Give the extent of all uninfected red blood cells.
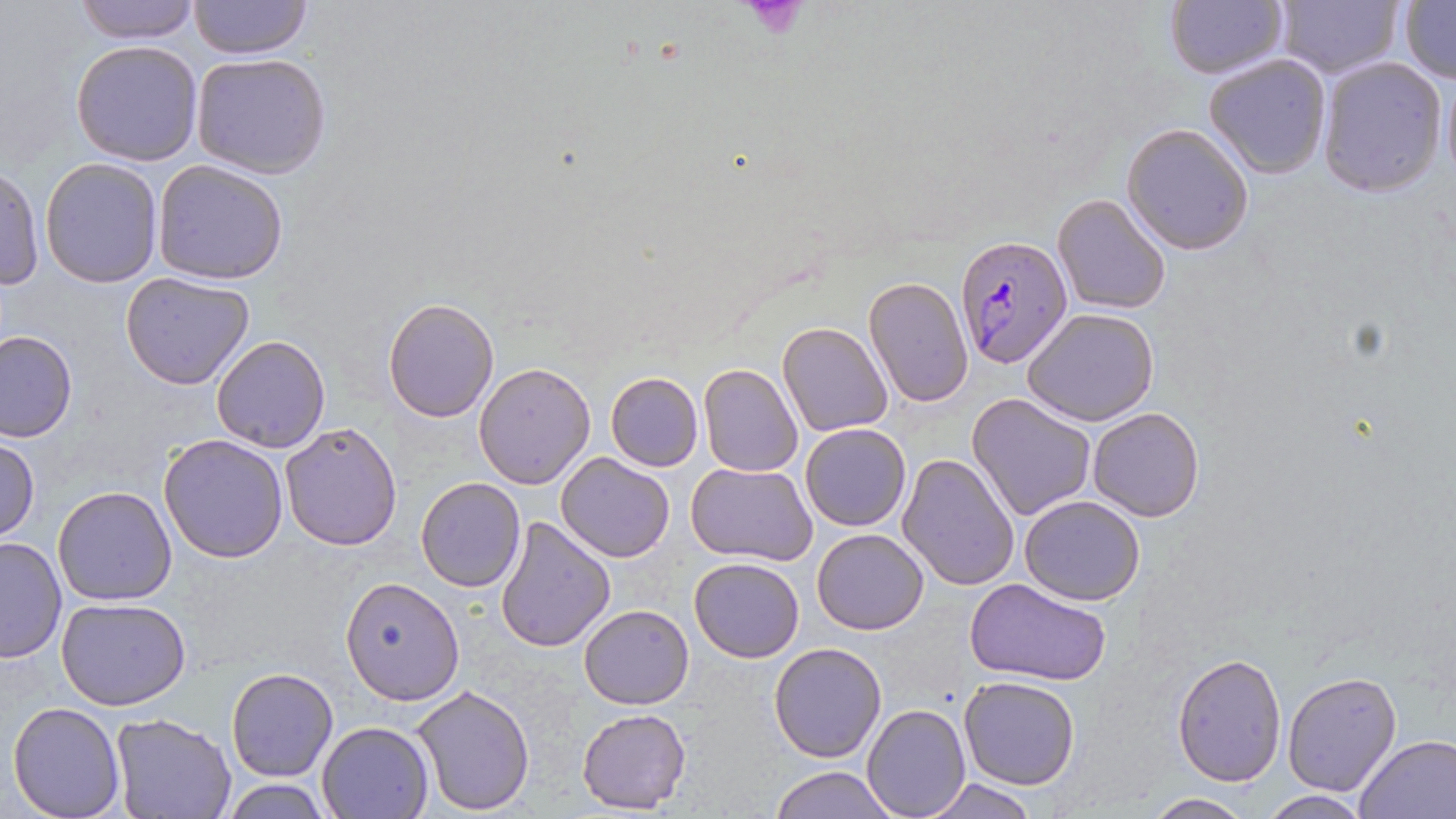
Approximate bounding boxes as (x1,y1)-(x2,y2) corner pairs in pixels.
Uninfected red blood cells: (70,0)-(204,43), (188,0)-(312,61), (1164,0)-(1288,81), (1272,1)-(1402,80), (1399,1)-(1456,85), (70,40)-(204,167), (190,52)-(332,178), (1202,53)-(1331,178), (1315,56)-(1447,197), (1122,123)-(1254,255), (41,158)-(163,287), (151,160)-(291,284), (1,162)-(43,294), (1052,193)-(1173,316), (119,271)-(256,389), (863,276)-(973,408), (384,298)-(498,422), (1023,308)-(1159,427), (777,320)-(893,437), (1,329)-(77,442), (212,335)-(330,453), (473,361)-(597,489), (698,364)-(804,476), (605,372)-(704,472), (967,393)-(1096,520), (1087,406)-(1205,522), (278,422)-(403,552), (799,423)-(911,531), (159,434)-(288,562), (1,436)-(39,541), (556,452)-(674,564), (897,454)-(1019,592), (685,462)-(817,565), (416,476)-(526,592), (53,486)-(178,605), (1020,495)-(1144,605), (495,515)-(615,653), (811,528)-(928,635), (0,536)-(65,665), (690,556)-(804,663), (963,576)-(1111,685), (342,577)-(464,703), (56,598)-(189,712), (579,603)-(694,709), (769,642)-(888,763), (1172,650)-(1288,785), (226,667)-(339,781), (1281,670)-(1402,796), (957,676)-(1082,790), (410,683)-(536,815), (859,698)-(1075,807), (7,701)-(125,819), (863,704)-(969,817), (576,708)-(690,813), (110,713)-(237,819), (315,720)-(435,818), (1354,733)-(1456,818), (768,764)-(895,819), (918,776)-(1041,818), (218,778)-(334,817), (1256,791)-(1374,818), (1143,792)-(1254,817).

Summary:
  - Plasmodium falciparum-infected red blood cell locations: (953,236)-(1072,368)
  - Platelet locations: (737,0)-(811,41)
  - Slide-level diagnosis: Plasmodium falciparum
  - Preparation: thin blood film
  - Image size: 1456×819 pixels
  - Magnification: 1000x
  - Field of view: one of a larger specimen
  - Stain: May-Grünwald-Giemsa
  - Modality: light microscopy